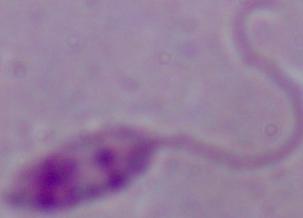

A Leishmania parasite is seen. Captured at 1000x magnification. Photomicrograph.